Outline each Plasmodium falciparum-infected red blood cell.
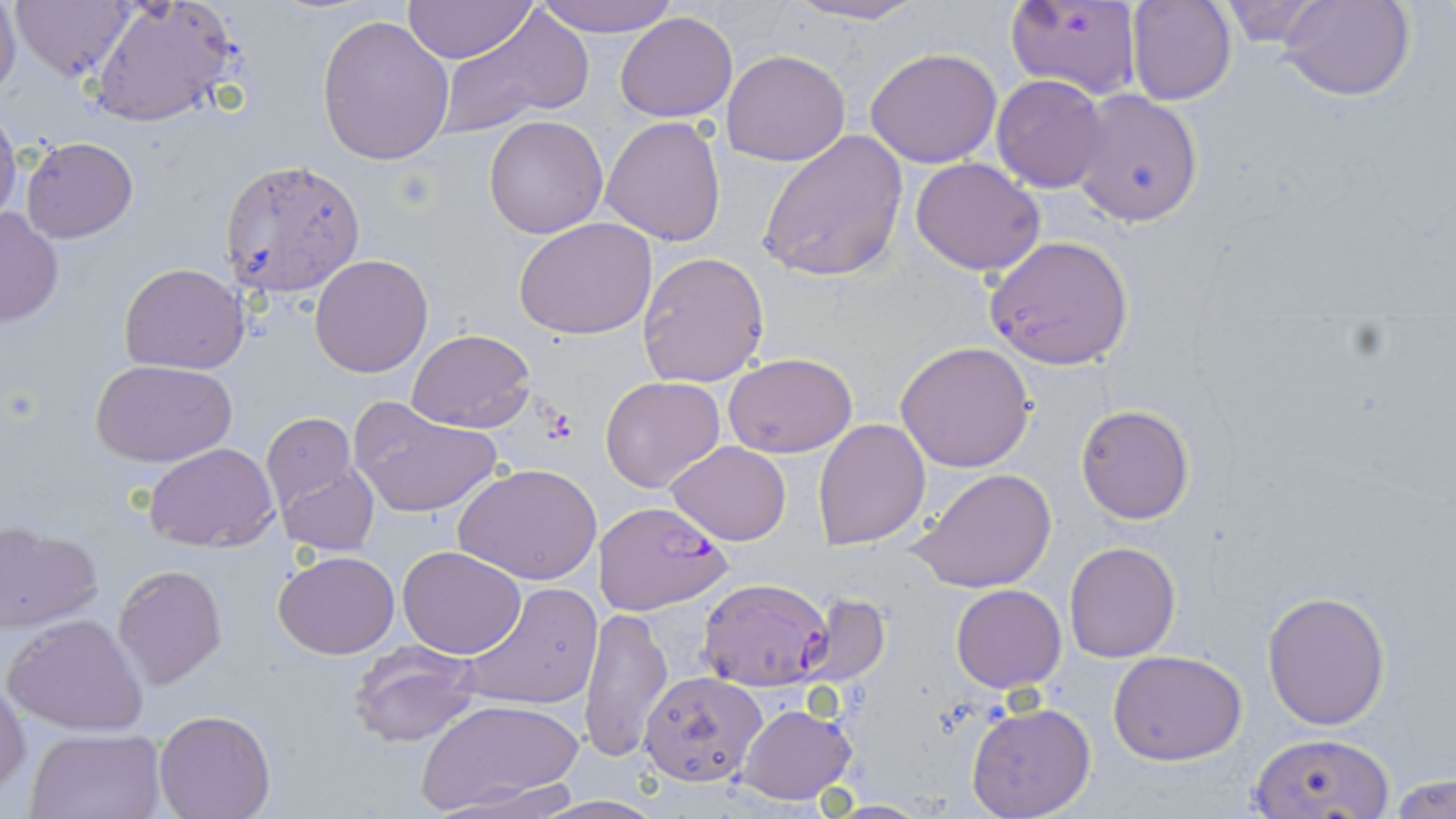

Approximate bounding boxes as (x1,y1)-(x2,y2) corner pairs in pixels.
Plasmodium falciparum-infected red blood cells: (594,499)-(733,614), (696,576)-(834,692), (639,670)-(765,786).

Summary:
  - Uninfected red blood cell locations: (0,0)-(21,100), (10,0)-(135,83), (532,0)-(679,39), (784,0)-(931,25), (1005,0)-(1143,100), (1126,0)-(1236,105), (1279,0)-(1415,102), (89,1)-(239,127), (403,1)-(535,65), (1213,1)-(1332,48), (438,7)-(592,135), (615,11)-(738,123), (317,15)-(455,166), (865,47)-(1004,168), (722,49)-(851,167), (992,73)-(1110,192), (1072,89)-(1203,226), (0,109)-(22,231), (484,114)-(609,238), (600,115)-(728,248), (758,129)-(909,284), (22,137)-(138,241), (911,157)-(1047,276), (221,159)-(366,298), (0,208)-(63,328), (514,218)-(658,340), (983,235)-(1135,370), (638,251)-(769,389), (310,254)-(433,376), (119,262)-(249,374), (407,328)-(537,432), (894,341)-(1036,472), (723,353)-(857,456), (92,359)-(237,467), (600,375)-(725,492), (352,403)-(500,519), (1075,404)-(1195,524), (261,414)-(357,509), (811,418)-(931,551), (666,440)-(792,547), (146,442)-(279,550), (275,461)-(381,556), (455,462)-(601,586), (910,466)-(1057,595), (1,522)-(102,631), (1064,541)-(1181,663), (398,546)-(526,657), (273,551)-(401,658), (113,563)-(227,689), (456,581)-(604,712), (950,584)-(1066,692), (1261,589)-(1392,730), (794,593)-(891,688), (580,605)-(674,764), (5,612)-(149,735), (349,639)-(484,747), (1110,649)-(1247,766), (1,678)-(28,796), (419,698)-(583,818), (965,701)-(1096,819), (736,703)-(857,806), (153,711)-(274,819), (27,729)-(164,818), (1249,734)-(1393,817), (1387,772)-(1456,818), (431,779)-(576,815), (536,795)-(669,817), (825,800)-(933,817)
  - Platelet locations: (539,408)-(581,447)
  - Slide-level diagnosis: Plasmodium falciparum
  - Preparation: thin blood smear
  - Image size: 1456×819 pixels
  - Stain: May-Grünwald-Giemsa
  - Modality: optical microscopy
  - Magnification: 1000x
  - Field of view: single